Identify the parasite.
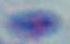
This is Toxoplasma gondii.

Summary:
  - Modality: micrograph
  - Magnification: 1000x